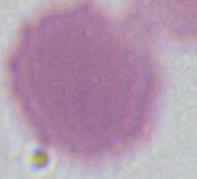

Summary:
  - Modality: photomicrograph
  - Magnification: 1000x
  - Identification: erythrocyte